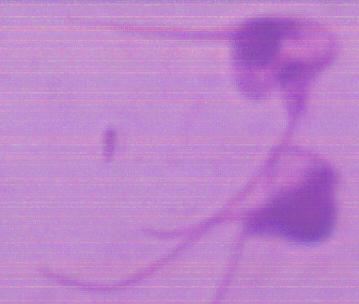
Summary:
  - Modality: photomicrograph
  - Identification: Leishmania
  - Magnification: 1000x